Assess the morphology of the red blood cells.
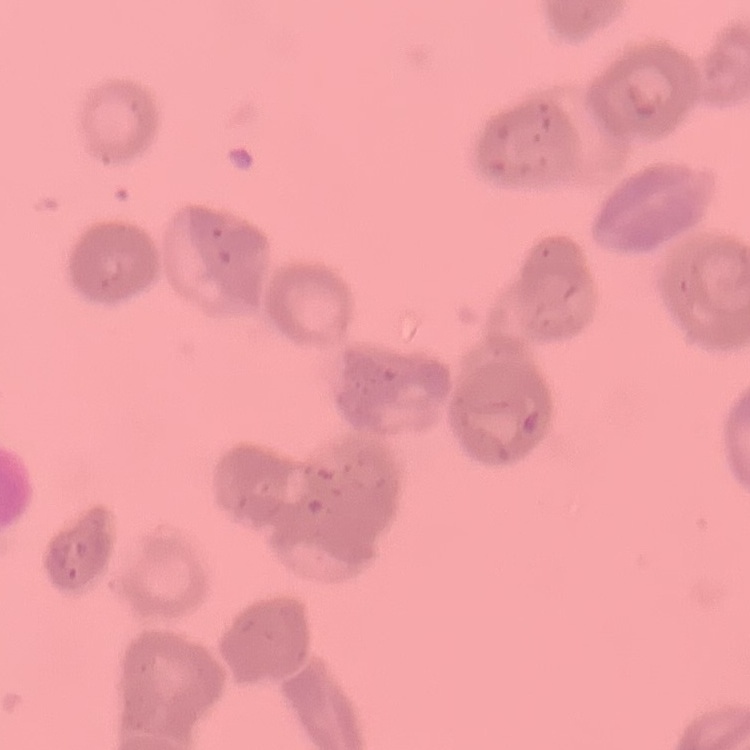

Rouleaux formation.

preparation = thin peripheral smear
image type = square crop of a larger photomicrograph
stain = Field's or Giemsa